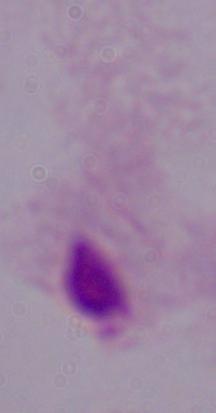

Summary:
  - Magnification: 1000x
  - Modality: photomicrograph
  - Identification: trichomonad